Locate the cells, classifying each as a parasitized red blood cell, an uninfected red blood cell, or a white blood cell.
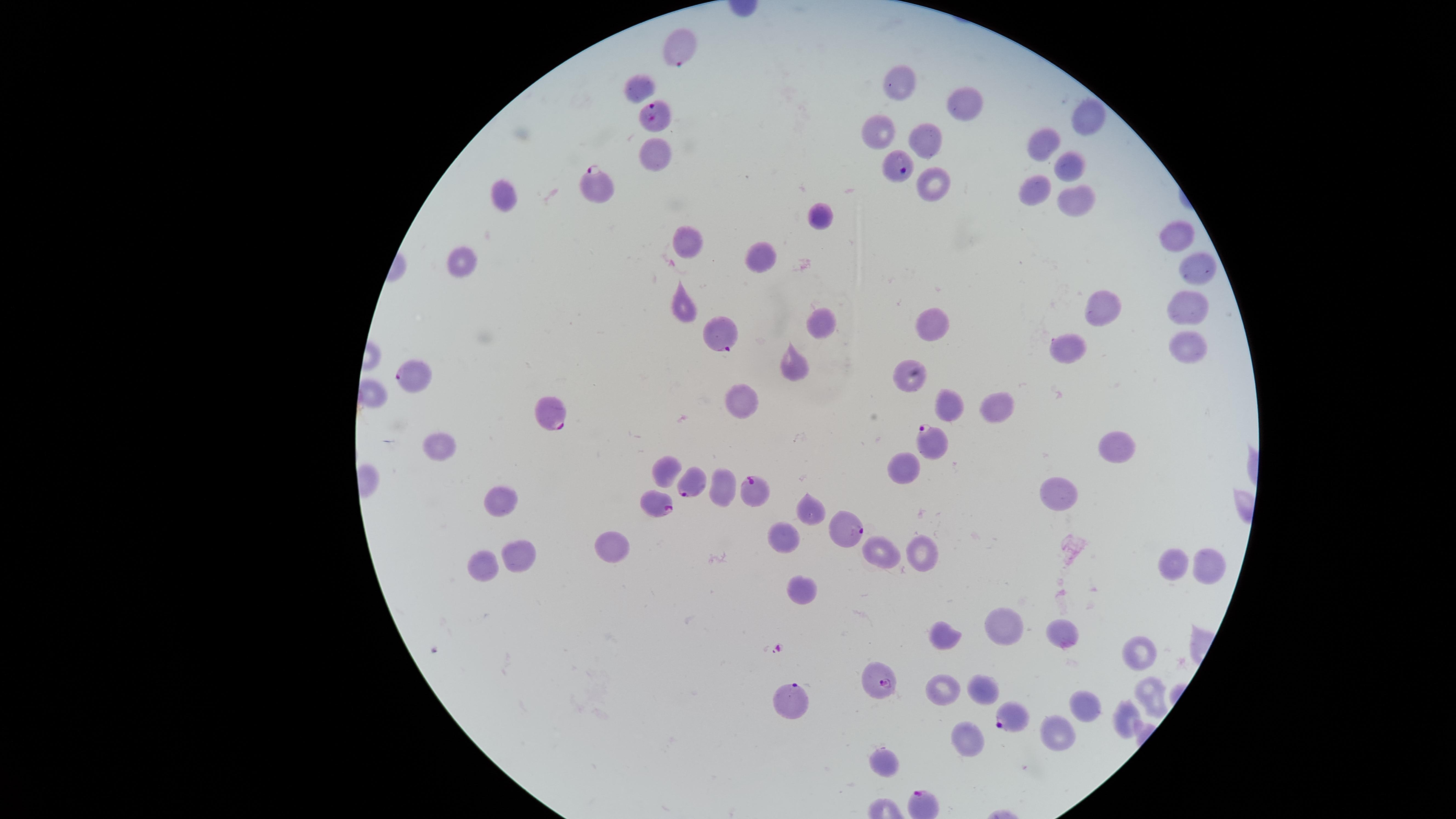

Approximate marker points as (x, y) in pixels.
Parasitized red blood cells: (681, 44), (656, 114), (593, 184), (726, 330), (415, 377), (553, 412), (936, 446), (689, 484), (757, 492), (656, 503), (844, 535), (880, 681), (789, 700), (1007, 716).
Uninfected red blood cells: (899, 82), (636, 90), (963, 101), (1091, 119), (877, 129), (924, 135), (1046, 141), (652, 152), (1069, 165), (937, 186), (1032, 190), (510, 193), (1076, 194), (823, 217), (1173, 234), (688, 237), (757, 252), (1197, 262), (463, 265), (1190, 300), (683, 302), (1108, 306), (821, 323), (936, 324), (1185, 344), (1073, 345), (790, 366), (908, 377), (747, 398), (954, 401), (1000, 401), (434, 444), (1116, 445), (909, 462), (664, 469), (718, 488), (1059, 489), (502, 499), (811, 511), (787, 536), (611, 549), (914, 551), (876, 554), (522, 559), (1204, 563), (1169, 565), (479, 567), (802, 592), (1005, 622), (947, 637), (1060, 638), (1139, 651), (941, 690), (981, 692), (1153, 697), (1089, 707), (1125, 723), (1056, 735), (961, 741), (885, 767).
No white blood cells identified.

Thin blood smear. Species: Plasmodium falciparum. Single field of view. The visible region is circular. Photographed with a smartphone camera through the microscope eyepiece. Image is 1456×819 pixels. Giemsa-stained preparation.